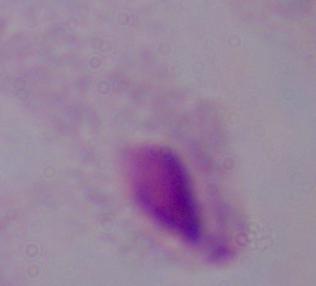

A trichomonad is shown. Captured at 1000x magnification. Micrograph.